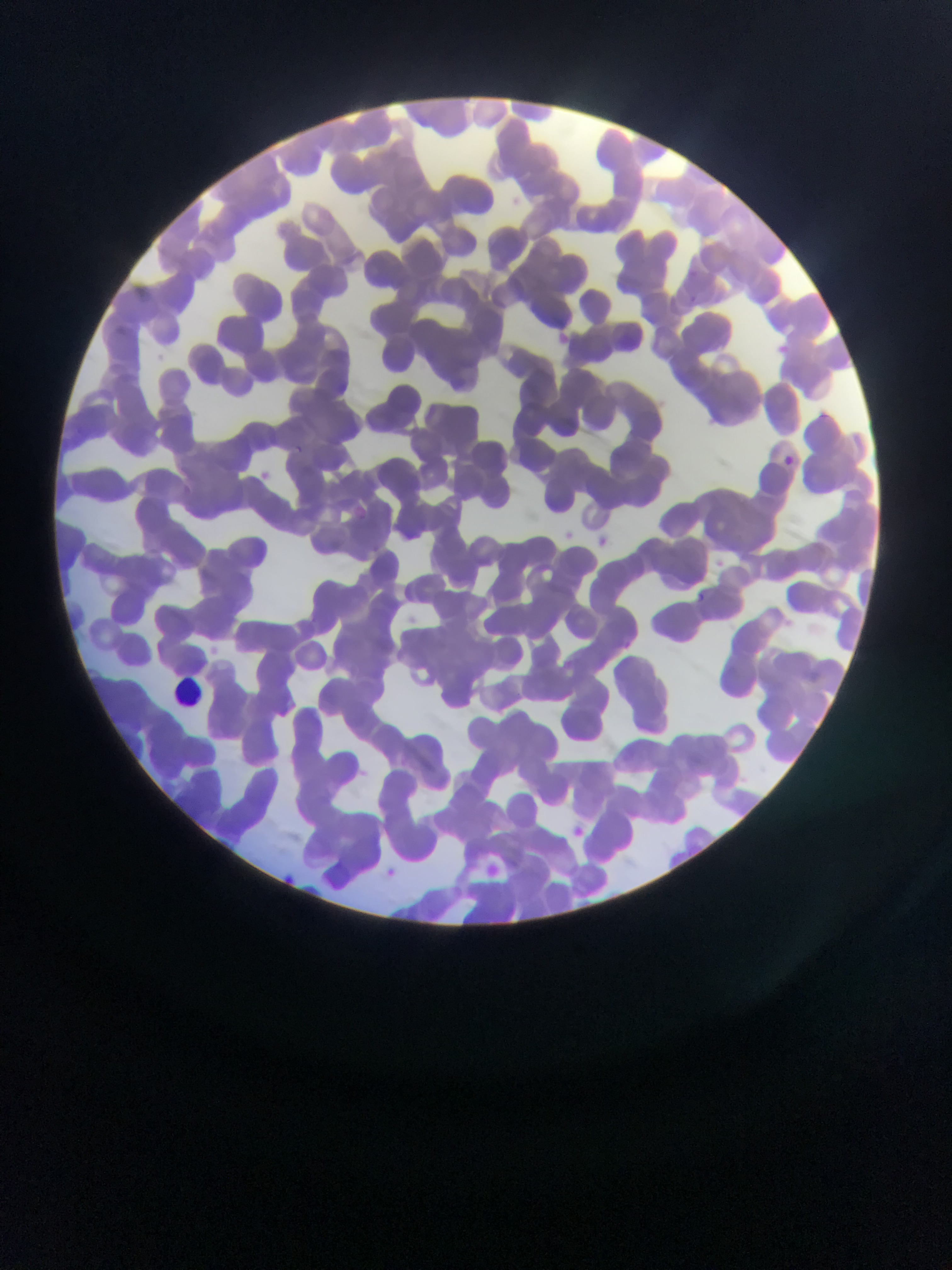

malaria parasite locations = approximate bounding boxes as [left, top, right, bottom] in pixels: [690, 290, 704, 311], [288, 443, 307, 459], [781, 454, 796, 467], [349, 506, 359, 517], [371, 537, 391, 552], [697, 589, 711, 602], [620, 633, 637, 651], [560, 820, 592, 847], [476, 858, 505, 885], [381, 859, 401, 878], [273, 867, 300, 888]
country = Ghana
capture = mobile-phone photograph through a microscope
preparation = thin blood smear
leukocyte locations = approximate bounding boxes as [left, top, right, bottom] in pixels: [173, 671, 199, 707]
field of view = single
image size = 952×1270 pixels